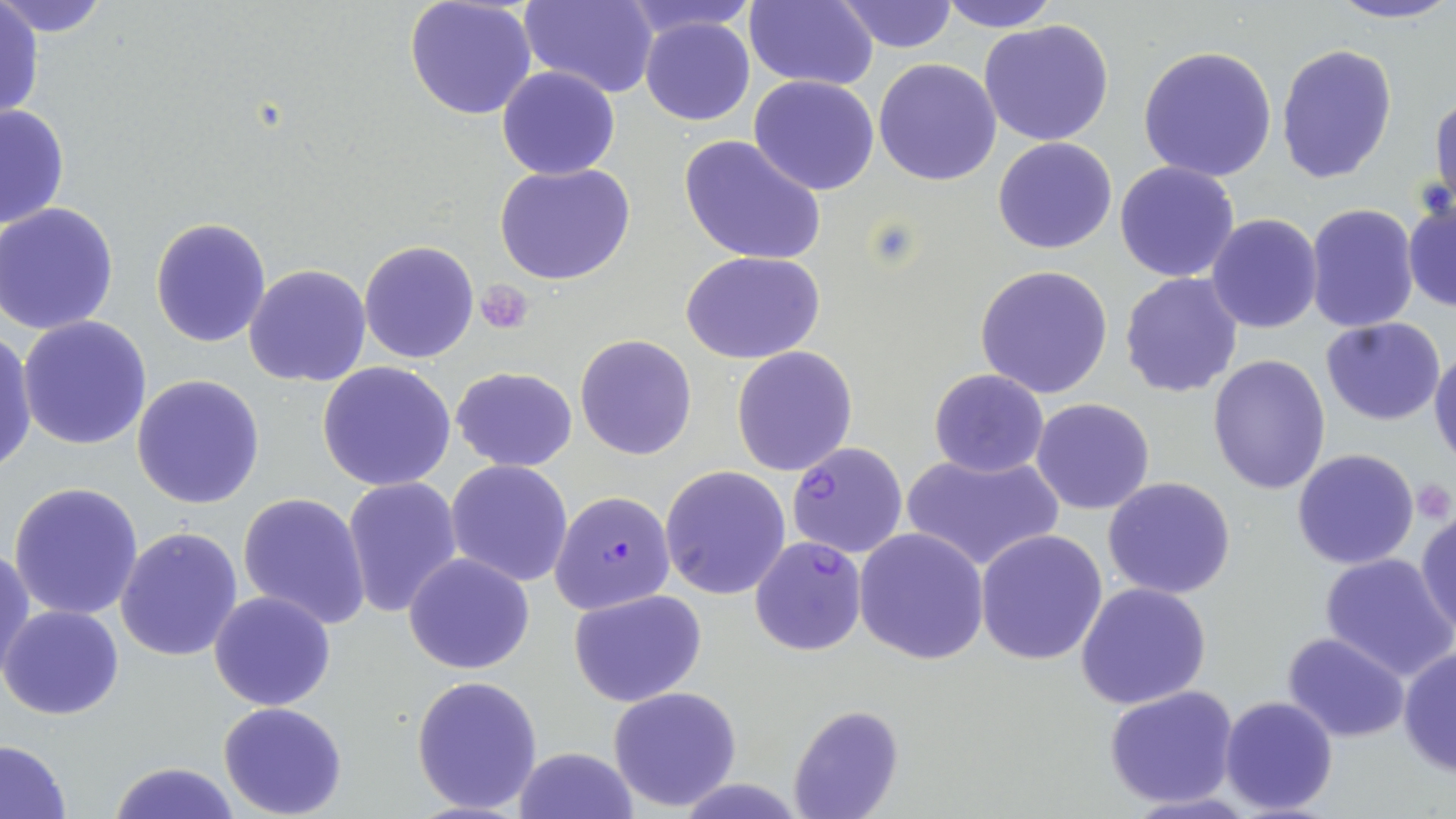 Approximate bounding boxes as [x1, y1, x2, y2] in pixels. Platelet locations: [477, 281, 532, 333], [1410, 479, 1452, 523]. Plasmodium falciparum-infected red blood cell locations: [786, 441, 908, 558], [550, 489, 675, 614], [749, 535, 868, 656]. Uninfected red blood cell locations: [0, 0, 110, 38], [404, 0, 537, 121], [523, 0, 660, 99], [622, 0, 756, 39], [744, 0, 879, 91], [937, 0, 1058, 31], [1323, 0, 1456, 26], [835, 1, 959, 53], [0, 3, 44, 121], [639, 15, 756, 126], [977, 20, 1116, 147], [1275, 43, 1397, 184], [1137, 44, 1278, 182], [873, 58, 1002, 187], [496, 65, 621, 180], [749, 76, 879, 194], [1430, 93, 1455, 212], [0, 104, 71, 233], [678, 136, 826, 266], [992, 136, 1119, 255], [1114, 161, 1240, 283], [493, 162, 636, 286], [1403, 200, 1456, 312], [1305, 203, 1420, 332], [1, 204, 121, 335], [1207, 213, 1322, 333], [150, 216, 272, 348], [359, 240, 479, 364], [681, 250, 826, 363], [243, 264, 371, 388], [974, 264, 1114, 399], [1119, 274, 1243, 398], [18, 315, 152, 451], [1319, 316, 1448, 425], [0, 330, 38, 476], [575, 334, 696, 460], [731, 345, 858, 477], [1429, 346, 1456, 467], [1207, 353, 1331, 495], [317, 361, 456, 491], [450, 365, 578, 472], [927, 368, 1050, 478], [132, 373, 265, 509], [1031, 398, 1156, 515], [1291, 448, 1420, 570], [901, 450, 1064, 574], [446, 460, 573, 587], [660, 464, 790, 599], [1103, 476, 1236, 602], [343, 477, 464, 620], [7, 480, 144, 621], [237, 491, 370, 629], [1415, 507, 1455, 639], [115, 526, 243, 662], [854, 528, 990, 666], [975, 528, 1108, 666], [0, 546, 35, 683], [403, 552, 535, 675], [1319, 552, 1456, 680], [1075, 582, 1211, 710], [567, 588, 707, 705], [208, 590, 337, 711], [2, 605, 124, 720], [1281, 633, 1411, 742], [1398, 648, 1455, 777], [412, 675, 544, 815], [608, 685, 743, 811], [1104, 685, 1241, 809], [1219, 695, 1338, 816], [217, 701, 349, 818], [789, 705, 904, 819], [0, 740, 72, 817], [511, 746, 636, 818], [106, 759, 244, 819]. Slide-level diagnosis: Plasmodium falciparum. May-Grünwald-Giemsa-stained preparation. Light microscopy. Captured at 1000x magnification. One field of a larger specimen. Image is 1456×819 pixels. Thin blood film.